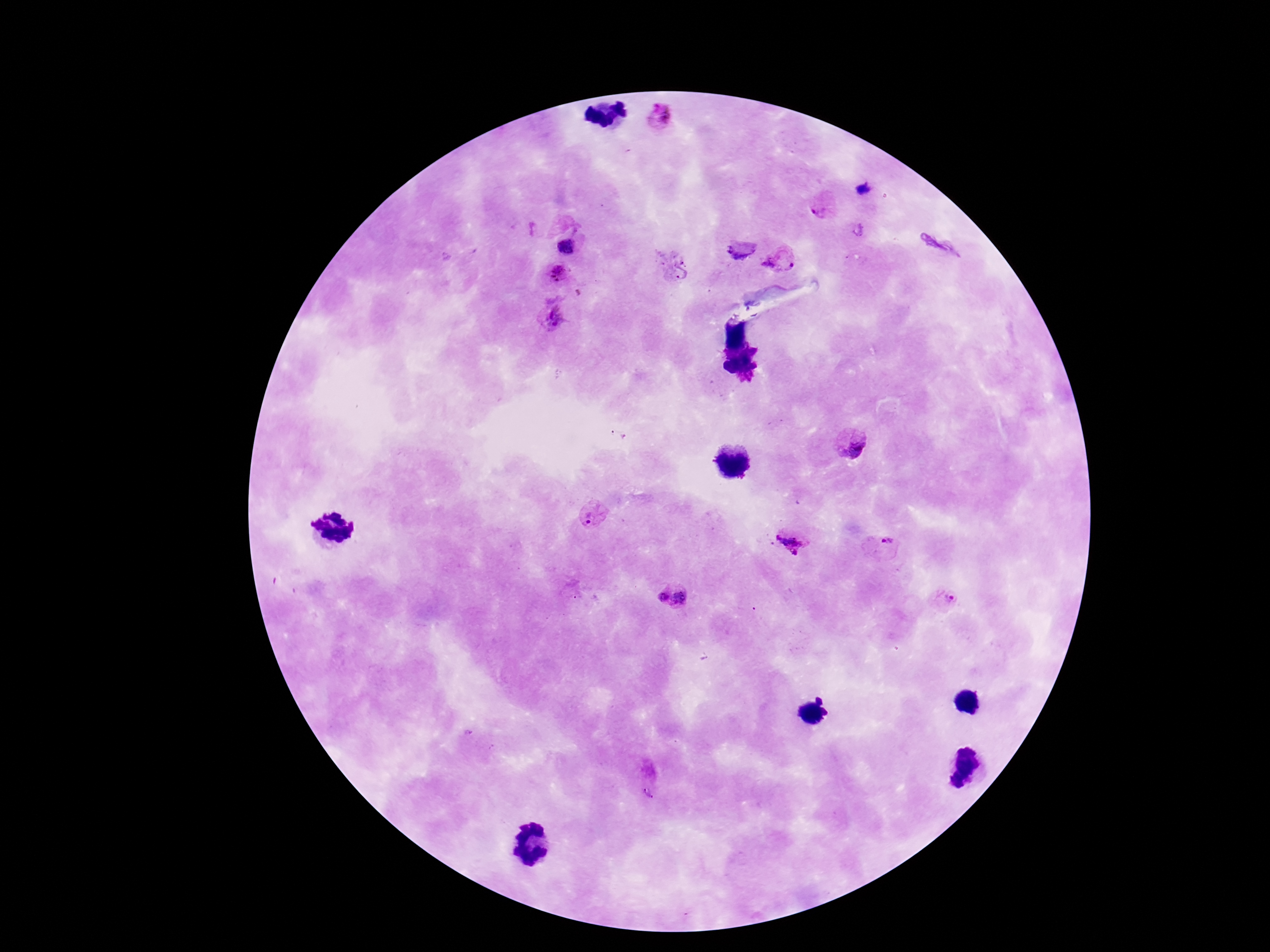
Approximate centers as (x, y) in pixels.
Summary:
  - Plasmodium parasite locations: (660, 116), (824, 206), (567, 244), (778, 262), (671, 266), (559, 273), (550, 320), (850, 445), (592, 516), (790, 543), (887, 545), (660, 596), (685, 597), (942, 598)
  - Preparation: thick blood film
  - Capture: smartphone camera through the microscope eyepiece
  - Magnification: 100x
  - Stain: Giemsa
  - Field of view: single
  - Patient malaria status: positive
  - Image size: 1270×952 pixels